Report the malaria status of this cell.
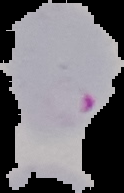
It is parasitized.

preparation = thin blood smear
image size = 124×193 pixels
image type = cell region segmented out of the field of view; surrounding area masked to black